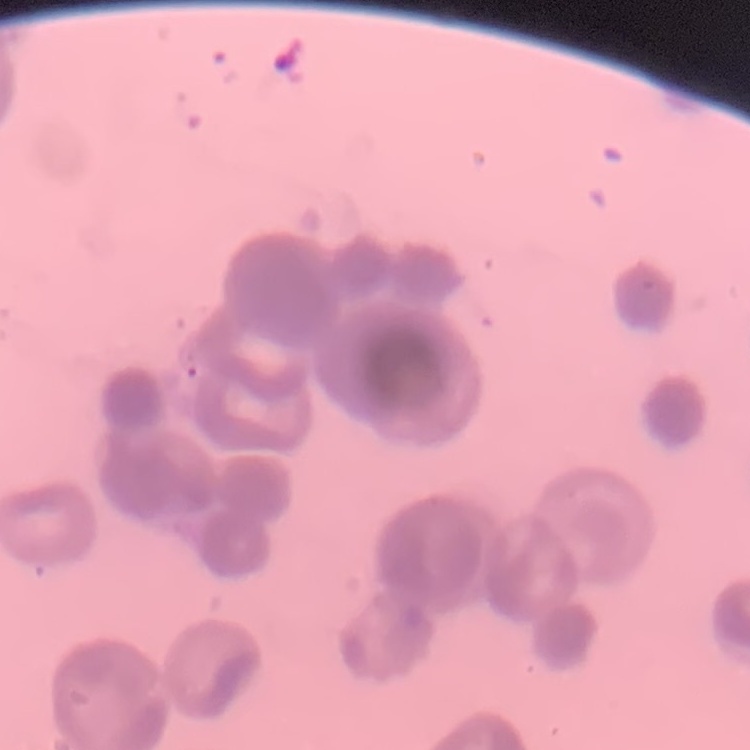
erythrocyte morphology = rouleaux formation
stain = Field's or Giemsa
image type = square crop of a larger photomicrograph
preparation = thin peripheral smear